State which parasite is depicted.
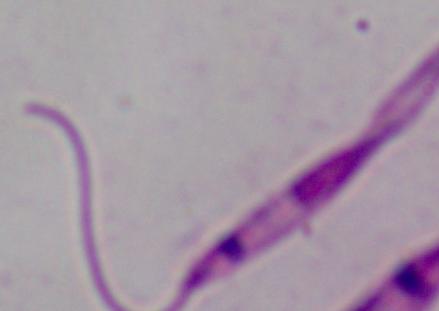
This is Leishmania.

Summary:
  - Modality: photomicrograph
  - Magnification: 1000x